Locate platelets.
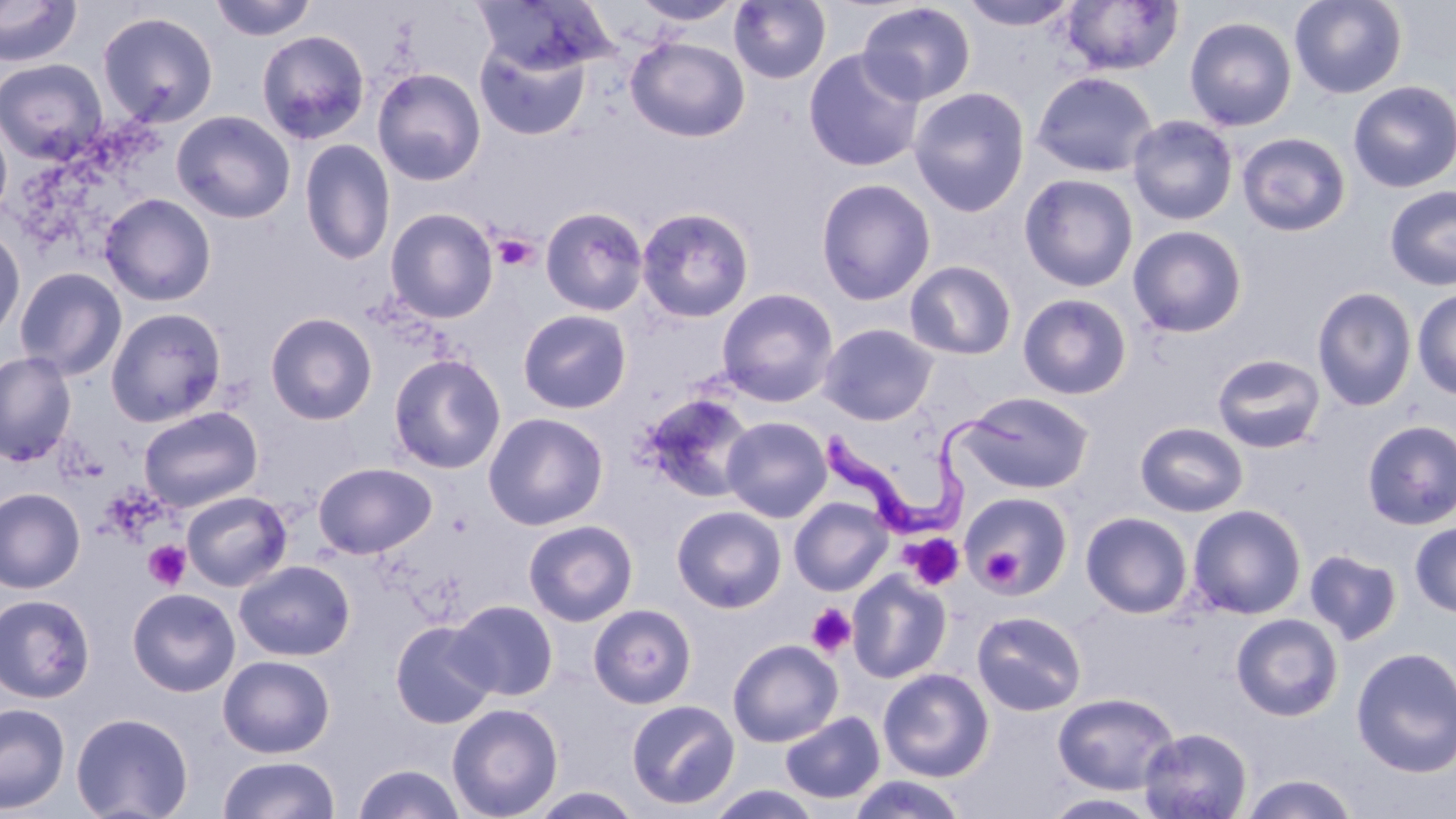
Approximate bounding boxes as (x1, y1, x2, y2) in pixels.
Platelets: (492, 234, 539, 271), (902, 533, 965, 591), (144, 540, 191, 590), (983, 548, 1024, 588), (806, 602, 856, 658).

Uninfected red blood cell locations: (0, 0, 82, 66), (210, 0, 318, 41), (631, 0, 743, 26), (729, 0, 831, 84), (957, 0, 1081, 31), (1289, 0, 1408, 99), (472, 1, 615, 76), (1060, 1, 1184, 75), (856, 2, 976, 105), (96, 11, 219, 127), (1184, 16, 1297, 132), (256, 30, 371, 145), (626, 36, 750, 143), (474, 40, 590, 141), (803, 49, 925, 172), (0, 58, 108, 164), (372, 67, 486, 186), (1031, 70, 1157, 178), (1348, 81, 1456, 193), (908, 86, 1030, 217), (172, 110, 296, 224), (1127, 114, 1238, 225), (0, 118, 13, 225), (1236, 132, 1351, 237), (299, 139, 396, 266), (1019, 173, 1139, 292), (815, 178, 936, 306), (1384, 184, 1456, 291), (99, 193, 216, 306), (541, 206, 649, 316), (385, 207, 499, 323), (636, 207, 754, 323), (0, 224, 26, 342), (1128, 225, 1247, 338), (904, 260, 1017, 360), (14, 266, 127, 380), (716, 287, 839, 407), (1312, 287, 1418, 411), (1412, 289, 1456, 400), (1017, 293, 1132, 399), (105, 307, 227, 426), (518, 309, 632, 414), (264, 312, 378, 425), (818, 323, 938, 425), (0, 351, 76, 466), (387, 353, 506, 474), (1212, 353, 1326, 453), (957, 391, 1094, 495), (639, 393, 758, 503), (138, 406, 263, 512), (483, 412, 609, 531), (721, 416, 832, 522), (1361, 420, 1456, 530), (1135, 422, 1249, 517), (312, 462, 436, 559), (0, 487, 85, 593), (180, 491, 292, 591), (959, 491, 1073, 599), (789, 497, 894, 596), (1188, 504, 1307, 619), (671, 505, 787, 613), (1080, 511, 1193, 618), (523, 519, 638, 626), (1409, 522, 1456, 618), (1304, 548, 1402, 645), (234, 559, 355, 661), (846, 570, 953, 684), (127, 588, 240, 697), (0, 594, 96, 704), (448, 599, 559, 701), (588, 604, 697, 708), (972, 610, 1086, 716), (1231, 613, 1344, 721), (389, 620, 498, 729), (727, 639, 843, 747), (1351, 646, 1456, 779), (217, 654, 336, 758), (878, 668, 994, 781), (1052, 691, 1180, 795), (626, 698, 740, 810), (0, 702, 70, 815), (446, 703, 564, 818), (779, 711, 885, 805), (71, 712, 193, 819), (1139, 727, 1253, 818), (217, 755, 341, 819), (352, 763, 466, 819), (1240, 774, 1360, 818), (846, 775, 968, 819), (705, 785, 824, 819), (527, 787, 645, 819), (1041, 792, 1161, 818). Trypanosoma brucei locations: (819, 400, 1034, 532). Slide-level diagnosis: Trypanosoma brucei. Light microscopy. 1000x magnification. One field of a larger specimen. May-Grünwald-Giemsa-stained preparation. Thin blood film. Image is 1456×819 pixels.